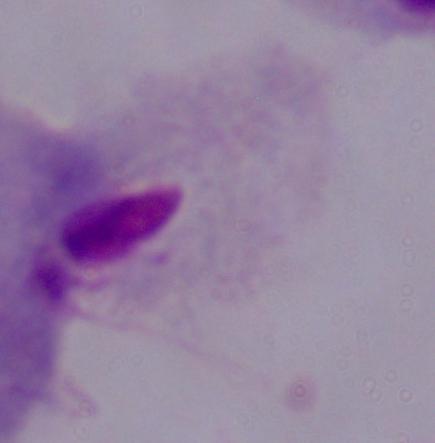
Captured at 1000x magnification. A trichomonad is seen. Photomicrograph.